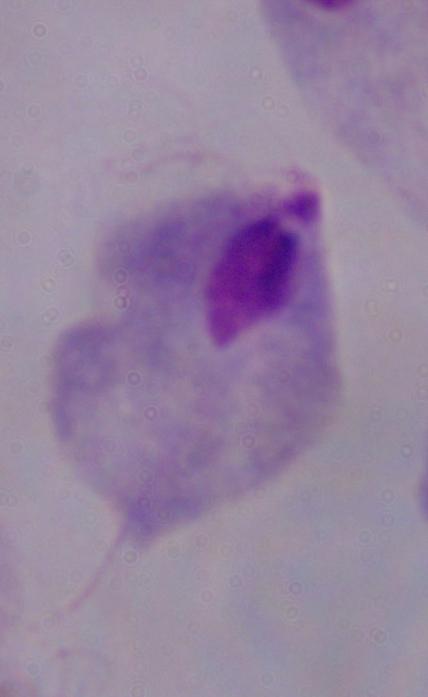

Captured at 1000x magnification. Micrograph. A trichomonad is shown.